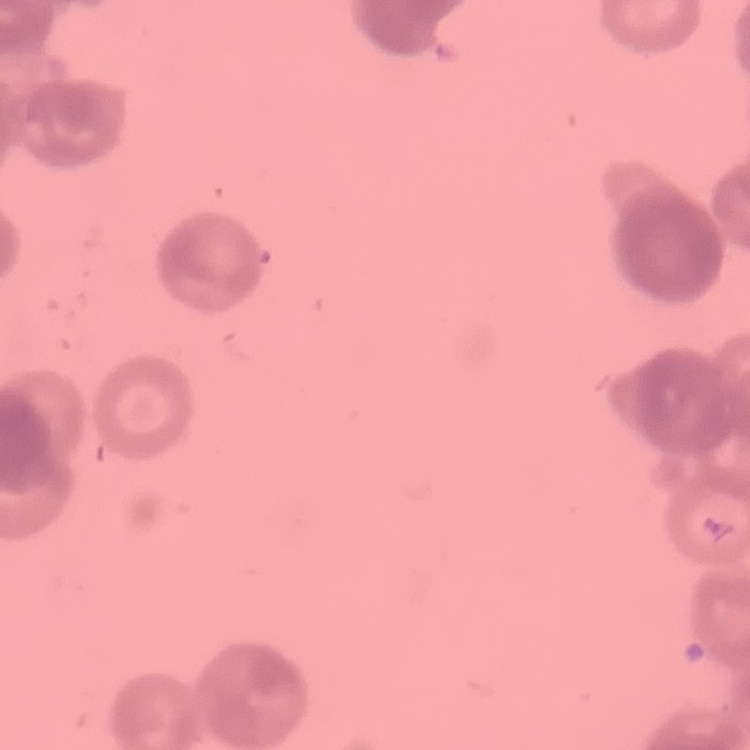

The red blood cells show rouleaux formation. Stained with either Field's or Giemsa. Thin peripheral smear. Square crop of a larger photomicrograph.